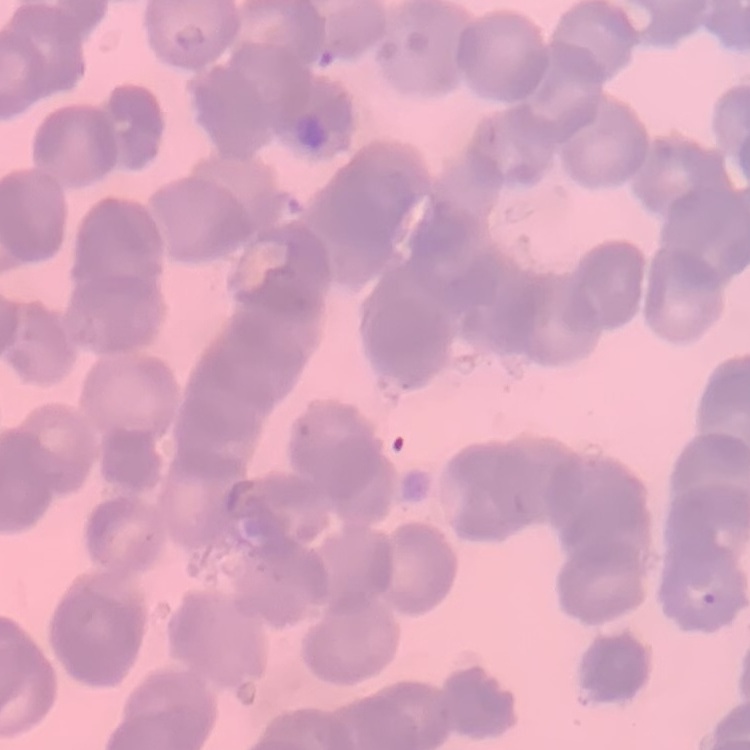

The red blood cells show rouleaux formation. Thin blood smear. One tile cut from a larger photomicrograph. Field's or Giemsa stain.